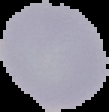
Summary:
  - Preparation: thin blood film
  - Malaria status: uninfected
  - Image type: segmented cell region on a black background
  - Image size: 109×112 pixels